Classify this cell by malaria status.
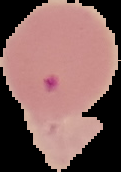
Parasitized.

The area outside the segmented cell region is set to black. From a thin blood smear. Image is 121×172 pixels.